Report the malaria status of this cell.
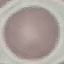
Uninfected.

Summary:
  - Image type: automatically extracted cell patch, resized to 64 × 64 pixels
  - Stain: Giemsa
  - Preparation: thin blood film
  - Capture: smartphone through the microscope eyepiece